Give the extent of all Plasmodium malariae-infected red blood cells.
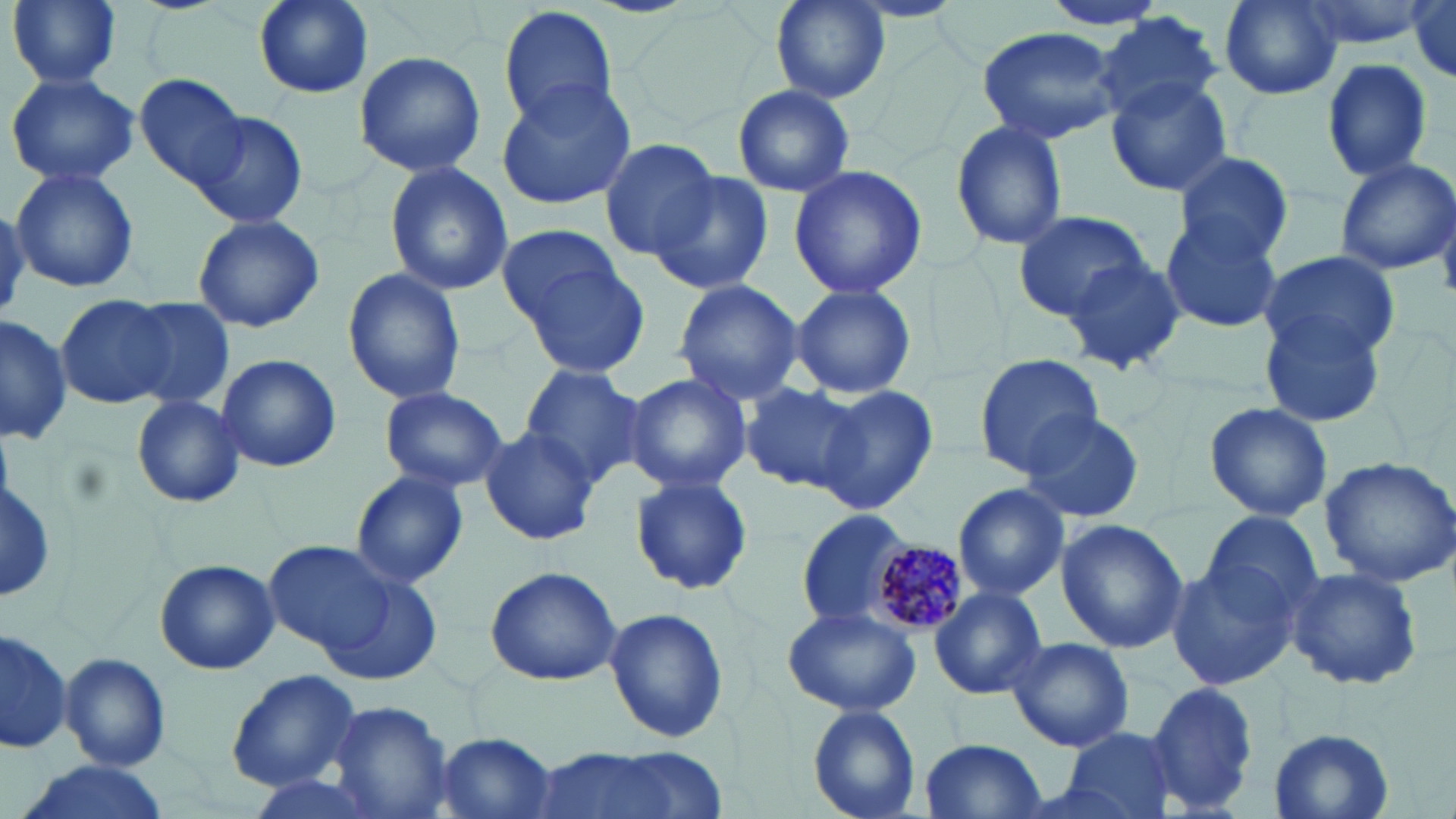
Approximate bounding boxes as (x1,y1)-(x2,y2) corner pairs in pixels.
Plasmodium malariae-infected red blood cells: (861,533)-(974,639).

Uninfected red blood cell locations: (8,0)-(121,89), (250,0)-(377,99), (769,0)-(889,103), (1216,0)-(1345,101), (1289,0)-(1431,50), (1407,0)-(1456,81), (1038,1)-(1172,31), (498,6)-(621,133), (1096,13)-(1221,123), (976,24)-(1121,145), (353,51)-(486,176), (1321,58)-(1432,180), (5,70)-(141,187), (136,72)-(252,192), (1105,76)-(1234,197), (496,79)-(638,208), (733,84)-(855,198), (188,110)-(307,230), (950,121)-(1068,250), (597,137)-(722,262), (1173,151)-(1295,263), (1334,157)-(1455,277), (384,162)-(513,294), (789,165)-(927,300), (10,168)-(140,294), (650,170)-(774,297), (1013,210)-(1154,319), (1159,213)-(1284,334), (190,214)-(327,334), (496,224)-(632,333), (1058,252)-(1185,375), (1257,252)-(1399,362), (517,259)-(652,380), (341,266)-(466,408), (672,278)-(805,407), (790,284)-(916,400), (58,295)-(179,408), (123,297)-(237,412), (0,313)-(70,449), (1260,316)-(1386,427), (217,352)-(342,473), (974,354)-(1107,476), (515,363)-(650,488), (621,371)-(752,496), (741,381)-(863,496), (377,385)-(508,494), (816,386)-(939,513), (129,393)-(248,508), (1204,399)-(1332,523), (1018,408)-(1146,523), (480,427)-(599,546), (1318,455)-(1456,585), (350,470)-(469,587), (629,472)-(753,596), (951,484)-(1069,601), (795,509)-(913,629), (1197,510)-(1323,629), (1054,519)-(1188,652), (262,540)-(405,662), (155,558)-(280,676), (1164,558)-(1300,690), (1284,565)-(1424,689), (483,567)-(623,686), (928,586)-(1046,699), (780,605)-(922,716), (602,606)-(730,745), (0,626)-(71,755), (1005,635)-(1135,753), (59,652)-(172,769), (225,670)-(363,790), (1144,679)-(1257,817), (327,699)-(454,819), (806,704)-(922,818), (1064,726)-(1177,819), (1267,729)-(1394,817), (432,732)-(561,819), (918,738)-(1047,818), (535,747)-(691,819), (12,760)-(175,819). Slide-level diagnosis: Plasmodium malariae. One field of a larger specimen. Thin blood film. Optical microscopy. May-Grünwald-Giemsa-stained preparation. Image is 1456×819 pixels. Captured at 1000x magnification.